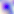 Toxoplasma gondii is seen. Captured at 400x magnification. Micrograph.